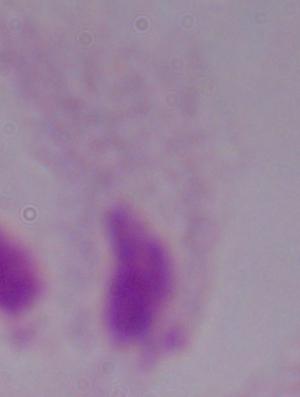
Summary:
  - Magnification: 1000x
  - Modality: photomicrograph
  - Identification: trichomonad